State which parasite is depicted.
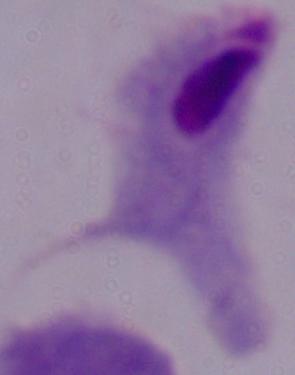

This is a trichomonad.

1000x magnification. Micrograph.